State which parasite is depicted.
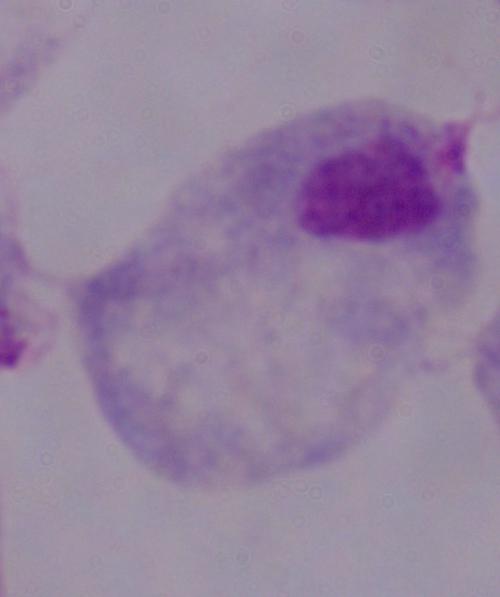
This is a trichomonad.

magnification = 1000x
modality = photomicrograph